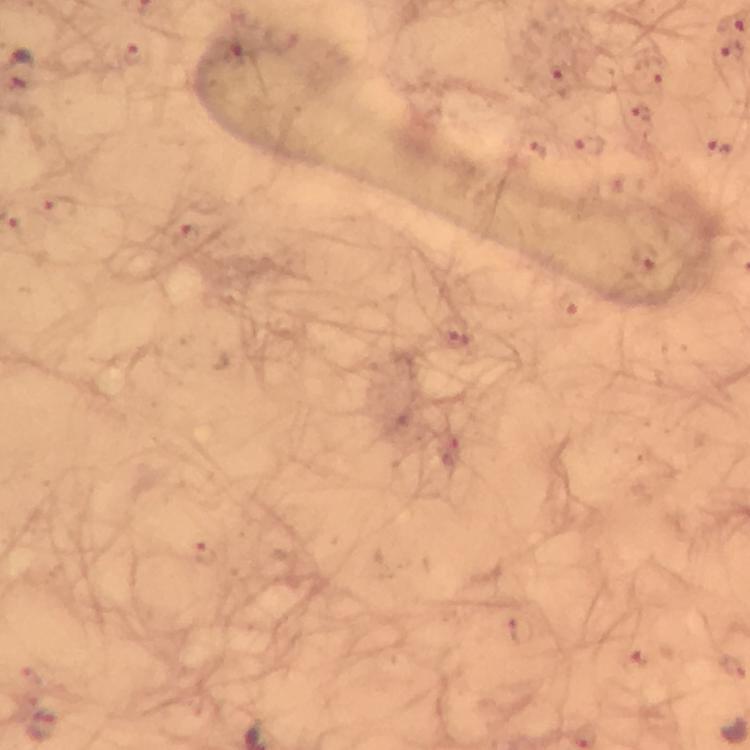

Approximate centers as (x, y) in pixels.
Summary:
  - Plasmodium parasite locations: (134, 56), (648, 76), (562, 78), (638, 120), (588, 145), (720, 149), (535, 151), (59, 206), (187, 237), (645, 257), (571, 304), (453, 331), (203, 553), (520, 630), (42, 725)
  - Magnification: 100x
  - Image size: 750×750 pixels
  - Immersion oil: applied
  - Context: from a diagnostic examination for malaria
  - Cropped from: one field of view
  - Preparation: thick blood film
  - Stain: Giemsa
  - Capture: smartphone photograph through a microscope